Outline each blood parasite and name the species.
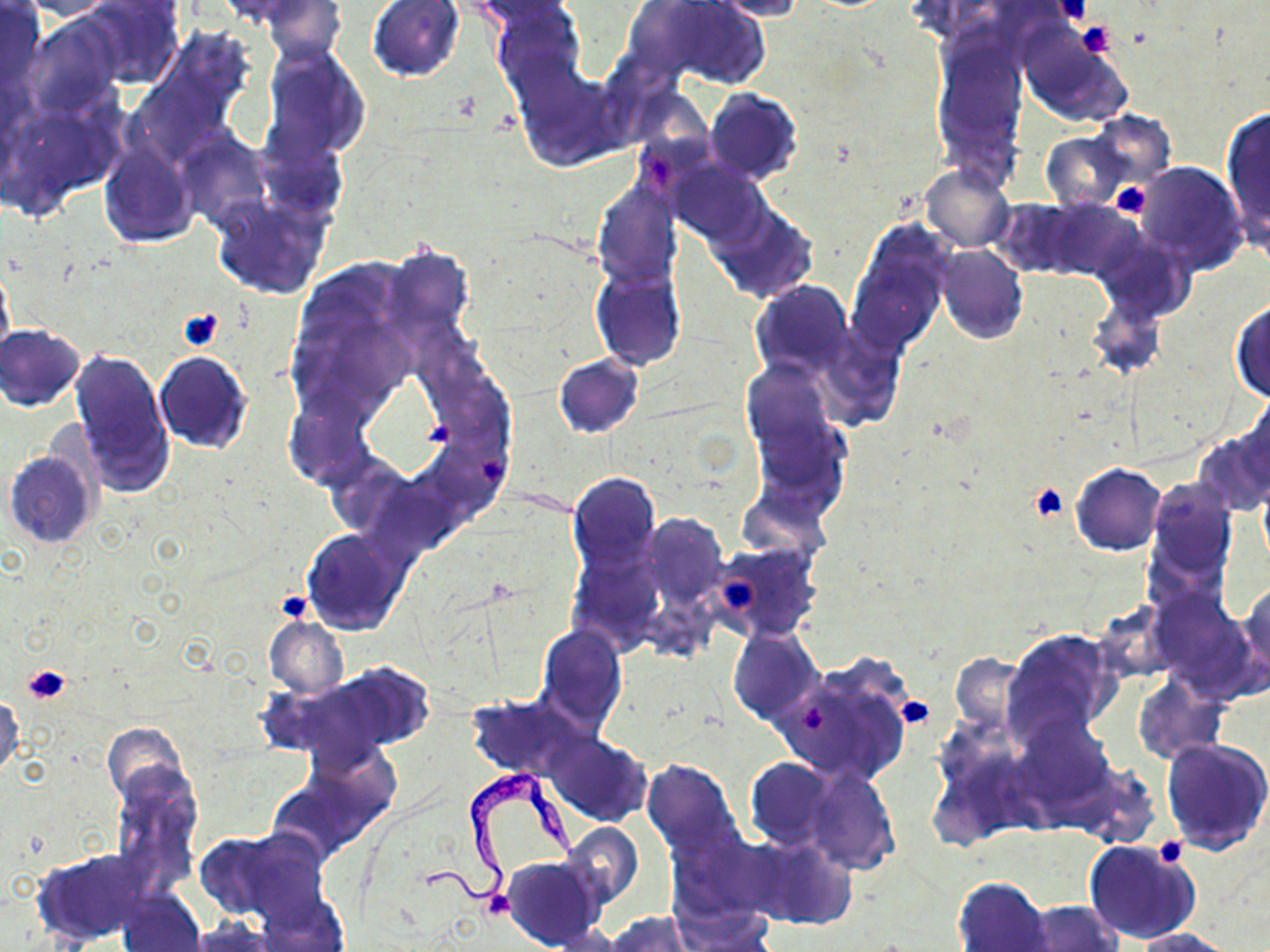
Approximate bounding boxes as (x1, y1, x2, y2) in pixels.
Trypanosoma brucei: (423, 769, 579, 909).
No Plasmodium falciparum, Plasmodium ovale, Plasmodium malariae, Plasmodium vivax, or Babesia divergens observed.

Summary:
  - Uninfected red blood cell locations: (0, 0, 46, 99), (15, 0, 120, 22), (80, 0, 183, 89), (215, 0, 338, 37), (468, 0, 582, 41), (633, 0, 770, 88), (708, 0, 809, 20), (257, 1, 346, 62), (368, 1, 465, 80), (493, 2, 584, 97), (28, 16, 121, 116), (1019, 31, 1132, 128), (931, 33, 1025, 173), (261, 49, 368, 168), (512, 63, 621, 170), (705, 88, 803, 184), (1221, 105, 1270, 240), (1085, 111, 1177, 193), (181, 133, 270, 226), (1041, 133, 1129, 211), (99, 142, 196, 247), (672, 162, 764, 246), (1133, 162, 1245, 270), (920, 164, 1014, 252), (592, 182, 681, 288), (212, 197, 328, 299), (990, 198, 1091, 277), (1039, 199, 1139, 281), (710, 205, 818, 302), (848, 227, 949, 353), (934, 245, 1028, 345), (382, 246, 472, 346), (1, 267, 14, 362), (593, 268, 685, 369), (751, 281, 852, 382), (1230, 299, 1270, 403), (1, 324, 85, 411), (70, 347, 173, 494), (154, 352, 251, 454), (554, 353, 644, 439), (740, 361, 837, 461), (1238, 396, 1270, 487), (750, 403, 846, 507), (1193, 428, 1270, 516), (4, 449, 99, 548), (1072, 463, 1165, 555), (567, 470, 660, 577), (1144, 479, 1237, 582), (644, 514, 728, 607), (301, 528, 408, 635), (711, 540, 822, 642), (1240, 583, 1269, 682), (1149, 591, 1255, 691), (265, 615, 348, 697), (535, 624, 628, 732), (728, 628, 823, 727), (1001, 629, 1120, 749), (950, 653, 1028, 735), (772, 661, 914, 787), (289, 663, 434, 761), (1132, 676, 1225, 765), (896, 691, 935, 730), (465, 693, 593, 783), (0, 696, 23, 780), (1009, 714, 1117, 819), (102, 721, 192, 813), (544, 732, 653, 828), (1161, 738, 1270, 856), (744, 757, 836, 851), (640, 758, 744, 860), (1069, 761, 1162, 847), (802, 763, 900, 876), (109, 767, 202, 893), (559, 821, 644, 911), (200, 827, 327, 926), (668, 829, 782, 919), (743, 835, 857, 931), (1083, 840, 1200, 945), (31, 849, 159, 946), (501, 855, 605, 950), (952, 876, 1054, 952), (116, 886, 206, 952), (256, 896, 349, 951), (1018, 900, 1122, 952), (603, 912, 696, 952), (1132, 926, 1238, 952)
  - Platelet locations: (1054, 0, 1090, 24), (1075, 20, 1115, 57), (1110, 184, 1154, 218), (176, 308, 224, 353), (479, 455, 504, 481), (1030, 484, 1070, 521), (723, 576, 757, 613), (275, 589, 314, 624), (22, 664, 72, 705), (894, 695, 932, 729), (800, 701, 827, 731), (1154, 835, 1187, 866), (479, 889, 515, 921)
  - Slide-level diagnosis: Trypanosoma brucei
  - Image size: 1270×952 pixels
  - Preparation: thin blood smear
  - Modality: optical microscopy
  - Magnification: 1000x
  - Field of view: one of a larger specimen
  - Stain: May-Grünwald-Giemsa